Locate every leukocyte (white blood cell).
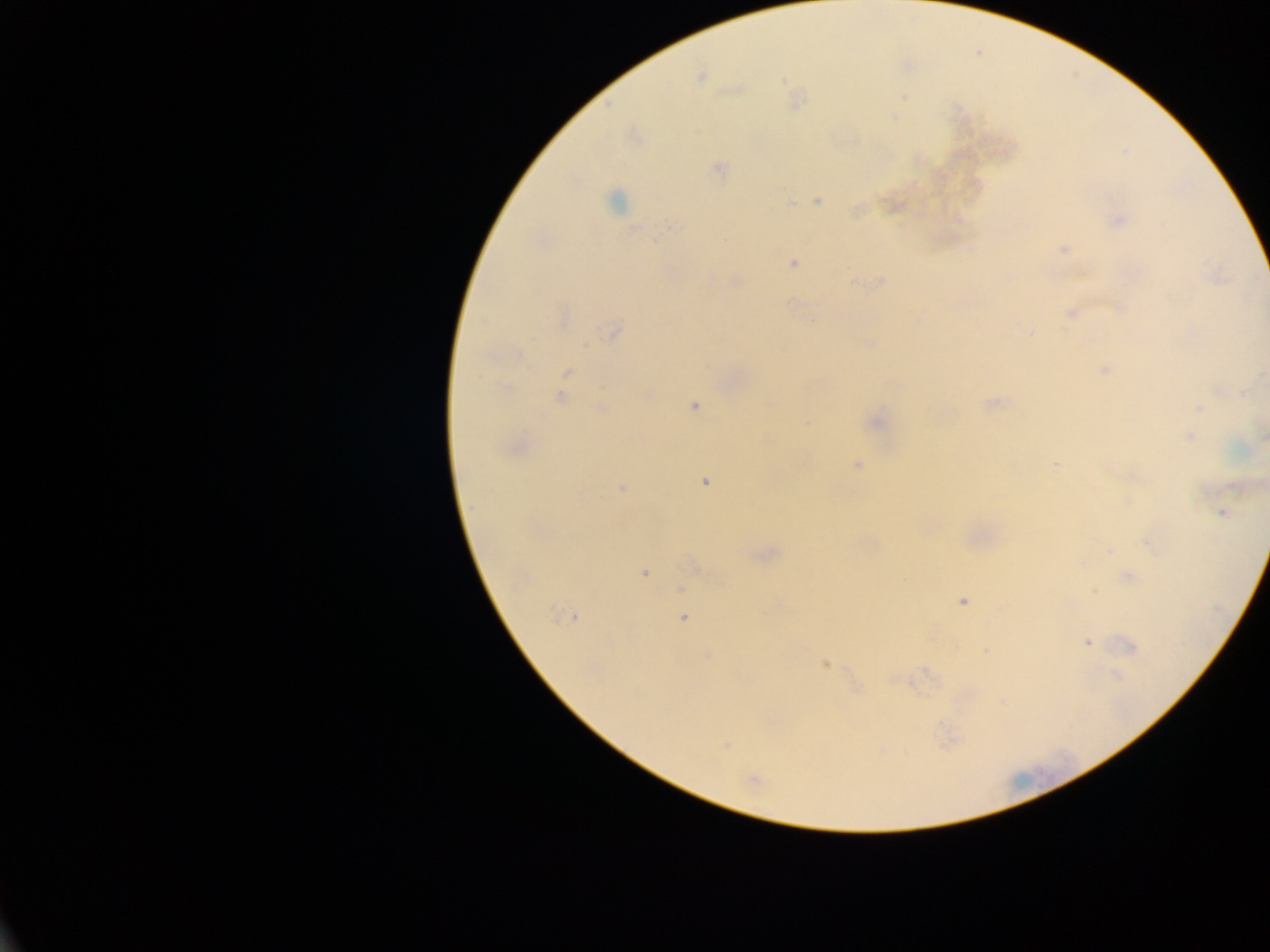

No leukocytes observed.

Approximate centers as [x, y] in pixels.
Summary:
  - Plasmodium parasite locations: [700, 77], [736, 90], [904, 97], [719, 168], [818, 200], [615, 202], [1118, 219], [670, 224], [1064, 249], [793, 263], [735, 280], [880, 282], [787, 302], [1071, 313], [564, 318], [614, 333], [518, 355], [1105, 370], [568, 372], [508, 388], [1220, 389], [560, 398], [771, 404], [992, 404], [694, 406], [603, 408], [1200, 408], [1190, 437], [1264, 437], [1055, 464], [857, 465], [705, 482], [623, 488], [1129, 501], [1222, 512], [1148, 543], [644, 573], [1129, 577], [681, 588], [964, 601], [566, 617], [684, 618], [1088, 643], [1132, 647], [987, 650], [825, 663], [1118, 675], [724, 745], [754, 780]
  - Country: Ghana
  - Capture: mobile-phone photograph through a microscope
  - Preparation: thick blood film
  - Field of view: single
  - Image size: 1270×952 pixels